Give the extent of all uninfected red blood cells.
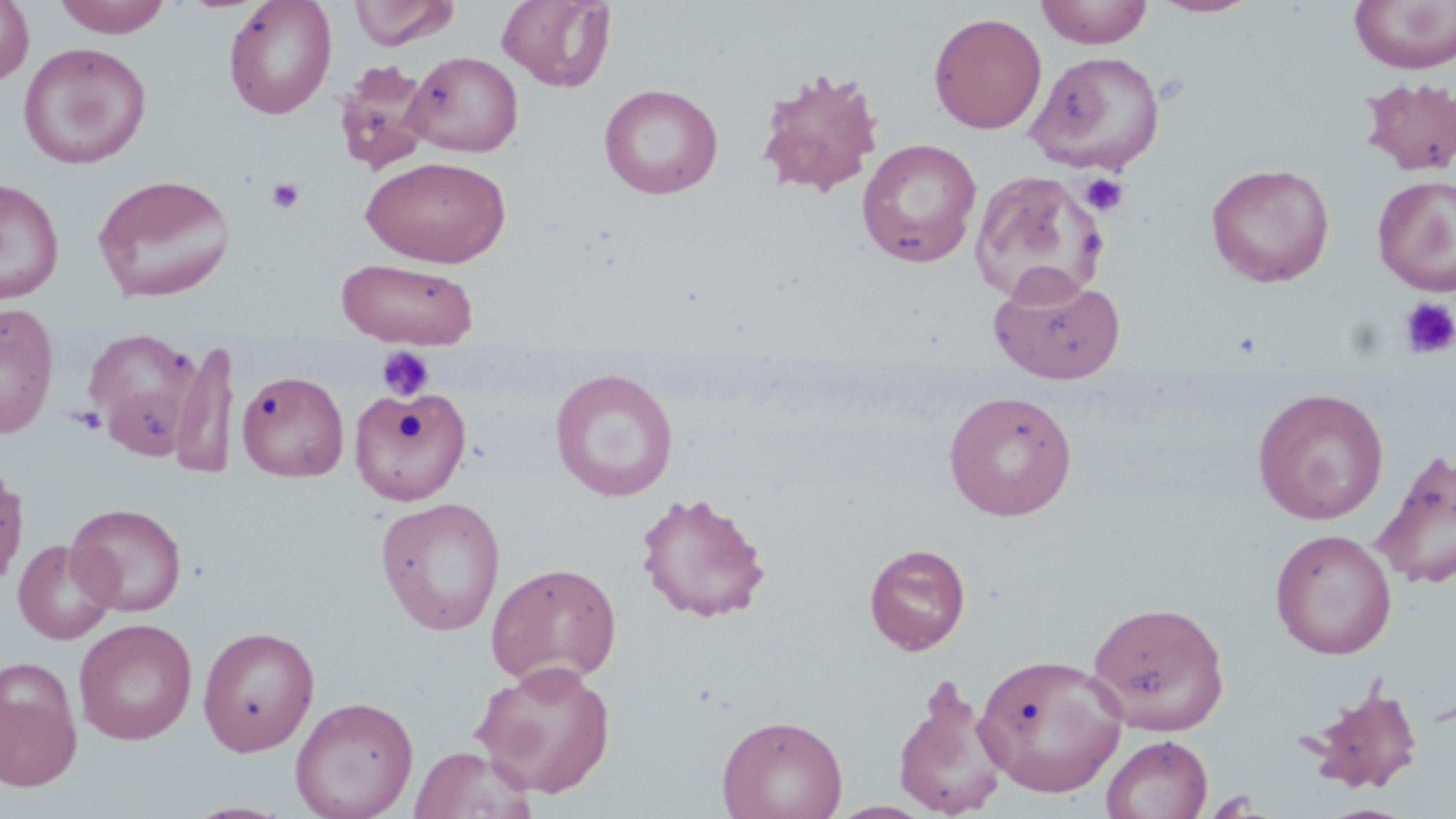

Approximate bounding boxes as named x1/y1/x2/y2 corners in pixels.
Uninfected red blood cells: (x1=0, y1=0, x2=35, y2=87), (x1=52, y1=0, x2=173, y2=37), (x1=222, y1=0, x2=337, y2=119), (x1=348, y1=0, x2=460, y2=50), (x1=496, y1=0, x2=617, y2=92), (x1=1035, y1=0, x2=1154, y2=48), (x1=1149, y1=0, x2=1263, y2=18), (x1=1349, y1=1, x2=1456, y2=74), (x1=928, y1=12, x2=1048, y2=134), (x1=18, y1=42, x2=152, y2=169), (x1=1026, y1=50, x2=1166, y2=174), (x1=405, y1=51, x2=524, y2=157), (x1=334, y1=59, x2=432, y2=174), (x1=755, y1=66, x2=885, y2=198), (x1=1358, y1=76, x2=1456, y2=177), (x1=597, y1=83, x2=724, y2=199), (x1=856, y1=138, x2=983, y2=268), (x1=361, y1=155, x2=511, y2=267), (x1=1205, y1=163, x2=1335, y2=287), (x1=969, y1=169, x2=1108, y2=306), (x1=92, y1=173, x2=236, y2=303), (x1=1372, y1=175, x2=1456, y2=295), (x1=0, y1=177, x2=65, y2=305), (x1=336, y1=257, x2=480, y2=349), (x1=989, y1=268, x2=1127, y2=385), (x1=0, y1=302, x2=60, y2=438), (x1=81, y1=327, x2=204, y2=455), (x1=170, y1=338, x2=240, y2=479), (x1=549, y1=367, x2=679, y2=502), (x1=236, y1=370, x2=349, y2=482), (x1=349, y1=385, x2=472, y2=505), (x1=1252, y1=387, x2=1389, y2=524), (x1=943, y1=389, x2=1078, y2=521), (x1=1372, y1=449, x2=1456, y2=590), (x1=0, y1=464, x2=29, y2=591), (x1=634, y1=490, x2=772, y2=623), (x1=375, y1=496, x2=507, y2=636), (x1=67, y1=502, x2=187, y2=617), (x1=1270, y1=528, x2=1397, y2=659), (x1=12, y1=539, x2=117, y2=645), (x1=863, y1=543, x2=971, y2=655), (x1=485, y1=561, x2=623, y2=688), (x1=1086, y1=600, x2=1231, y2=735), (x1=74, y1=618, x2=197, y2=745), (x1=197, y1=625, x2=320, y2=756), (x1=974, y1=652, x2=1128, y2=797), (x1=0, y1=658, x2=83, y2=792), (x1=472, y1=660, x2=617, y2=797), (x1=892, y1=679, x2=1010, y2=819), (x1=1302, y1=682, x2=1425, y2=795), (x1=290, y1=695, x2=419, y2=819), (x1=716, y1=713, x2=848, y2=819), (x1=1101, y1=734, x2=1214, y2=819), (x1=410, y1=745, x2=537, y2=819), (x1=825, y1=800, x2=937, y2=818), (x1=1316, y1=803, x2=1420, y2=819).

Platelet locations: (x1=1080, y1=172, x2=1129, y2=217), (x1=266, y1=176, x2=307, y2=214), (x1=1399, y1=297, x2=1456, y2=359), (x1=375, y1=344, x2=436, y2=402), (x1=69, y1=406, x2=107, y2=435). Slide-level diagnosis: no evidence of blood parasites. Image is 1456×819 pixels. Single field of view. May-Grünwald-Giemsa-stained preparation. Thin blood film. Captured at 1000x magnification. Optical microscopy.